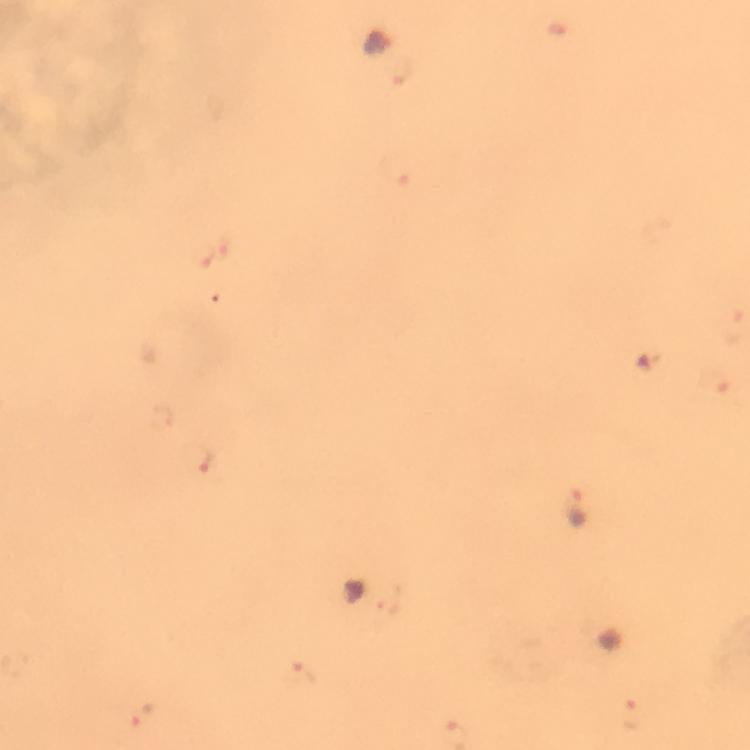
Approximate centers as {x, y} in pixels. Malaria parasite locations: {379, 43}, {203, 253}, {200, 460}, {579, 508}, {300, 675}, {630, 716}. Immersion oil applied. Image is 750×750 pixels. From a malaria diagnostic workup. Thick blood smear. Giemsa stain. 100x magnification. Photographed through the microscope with a smartphone camera. Cropped region of a single field of view.